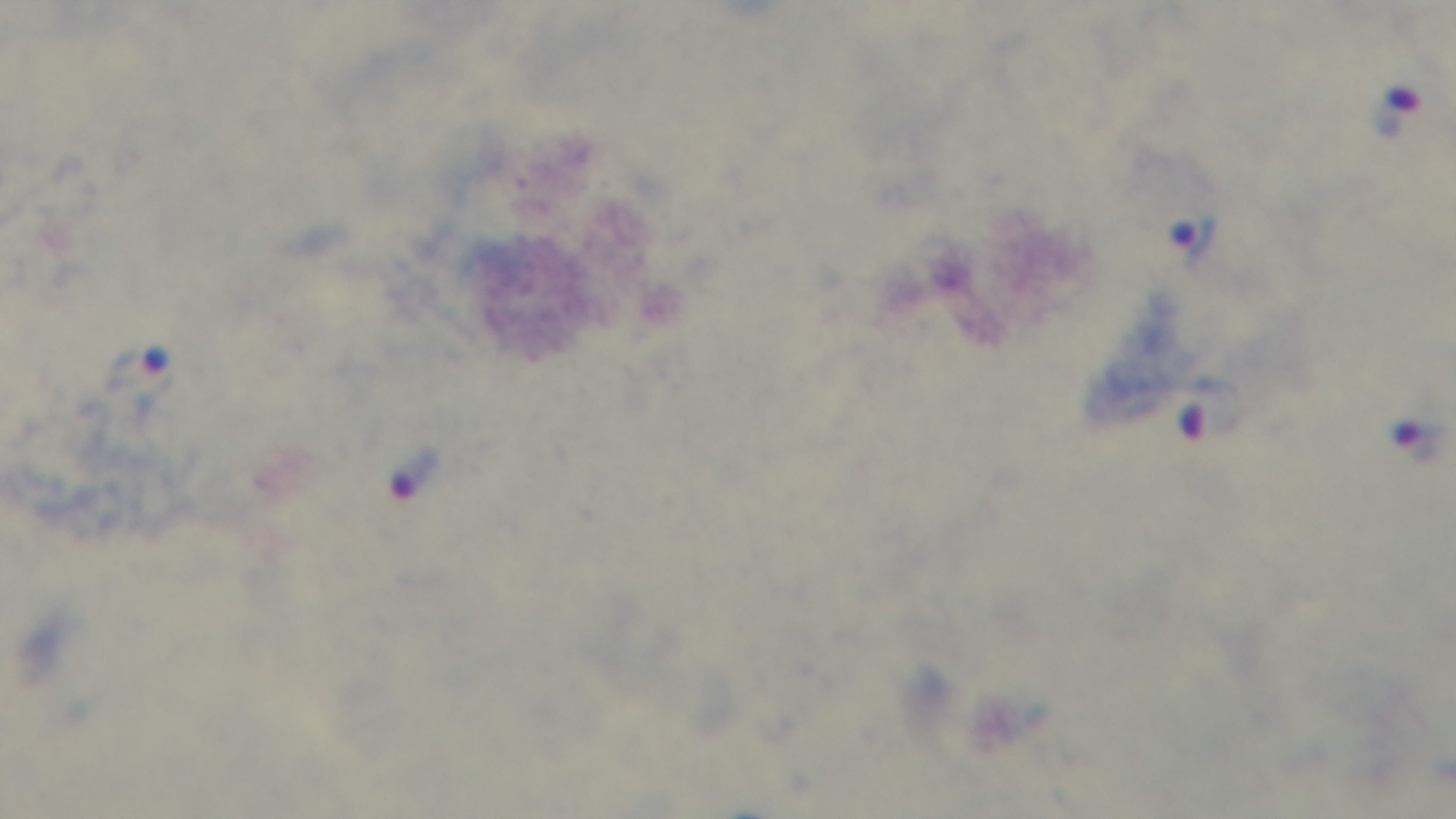

preparation = thick blood film
objective = 100x oil immersion
field of view = single
stain = Giemsa
malaria status = infected
capture = mounted 4K digital camera
modality = light microscopy